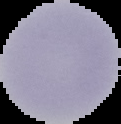

preparation: thin blood smear
image_type: segmented cell region with the area outside set to black
malaria_status: uninfected
image_size: 121×124 pixels